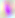 Photomicrograph. Toxoplasma gondii is seen. 400x magnification.